Locate every blood parasite and identify its species.
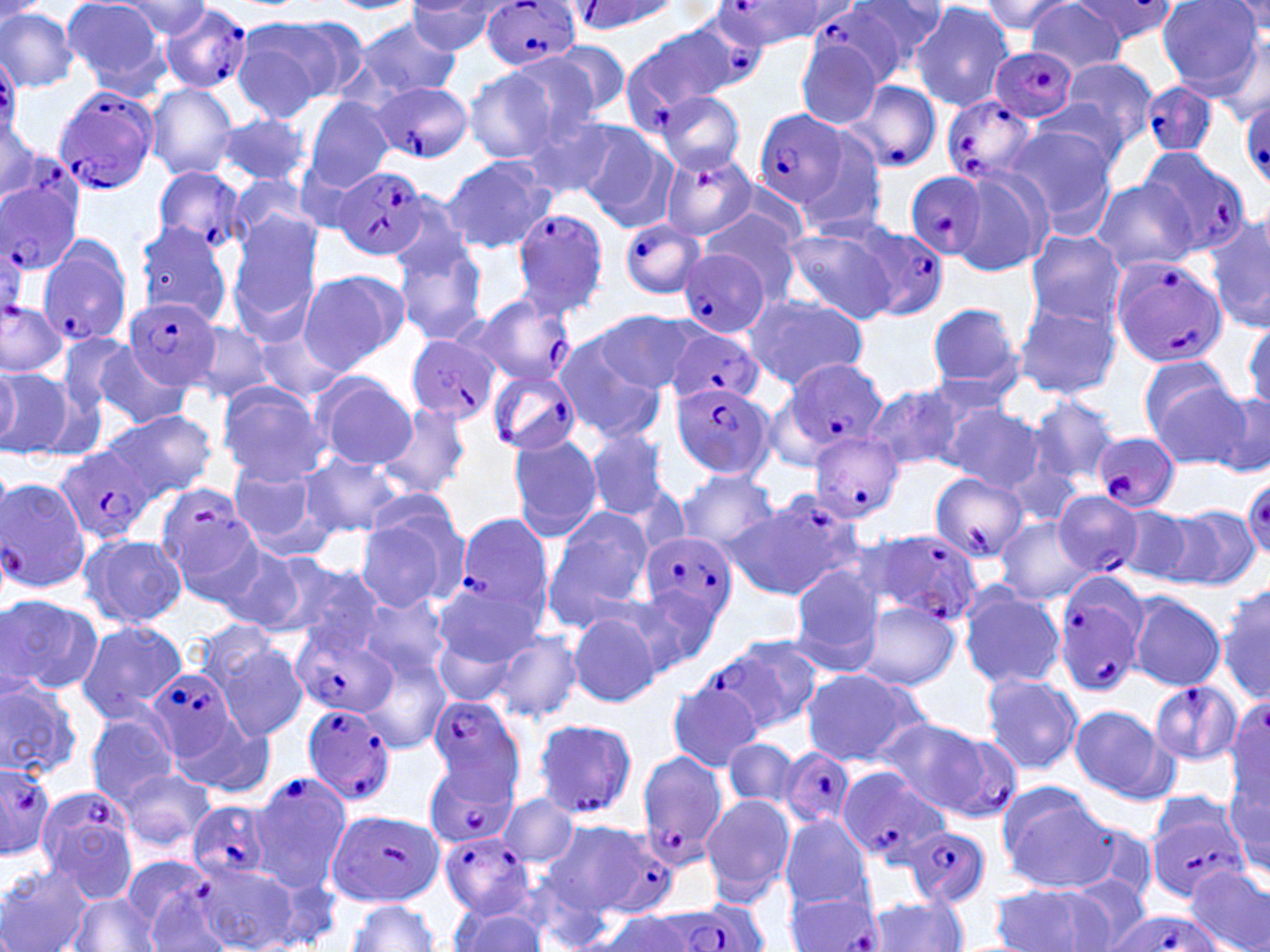

Approximate bounding boxes as (x1, y1, x2, y2) in pixels.
Plasmodium falciparum-infected red blood cells: (719, 0, 830, 50), (571, 1, 680, 33), (484, 2, 581, 72), (157, 5, 253, 94), (811, 6, 909, 87), (679, 10, 769, 93), (621, 27, 737, 124), (988, 47, 1079, 124), (0, 54, 22, 139), (843, 79, 943, 174), (365, 80, 474, 162), (1142, 81, 1216, 156), (51, 86, 160, 196), (942, 94, 1040, 186), (1239, 95, 1270, 187), (754, 110, 848, 208), (1140, 148, 1252, 253), (662, 152, 757, 242), (152, 166, 250, 255), (334, 168, 428, 260), (2, 169, 85, 277), (903, 172, 985, 262), (512, 208, 609, 318), (618, 219, 707, 301), (848, 224, 949, 319), (0, 230, 26, 325), (36, 236, 132, 348), (678, 247, 770, 337), (1110, 257, 1226, 368), (125, 296, 220, 391), (452, 297, 575, 400), (668, 331, 764, 408), (406, 334, 499, 424), (777, 358, 887, 460), (485, 367, 581, 457), (672, 381, 773, 482), (810, 432, 903, 524), (1093, 432, 1180, 513), (57, 446, 153, 548), (930, 471, 1030, 562), (2, 476, 91, 596), (154, 482, 258, 589), (1053, 491, 1144, 577), (453, 512, 552, 626), (639, 530, 738, 634), (855, 530, 984, 627), (1051, 573, 1147, 697), (292, 627, 396, 719), (717, 635, 824, 735), (146, 668, 241, 762), (1149, 680, 1242, 765), (425, 695, 527, 797), (301, 703, 398, 807), (530, 717, 639, 820), (932, 729, 1023, 824), (779, 749, 855, 830), (635, 750, 727, 870), (0, 760, 56, 856), (424, 761, 517, 849), (838, 770, 952, 866), (249, 773, 351, 890), (35, 785, 139, 902), (187, 800, 273, 882), (1146, 808, 1248, 902), (329, 811, 444, 907), (901, 825, 992, 910), (439, 830, 536, 918), (603, 833, 671, 913), (123, 856, 211, 934), (785, 892, 883, 951), (674, 900, 768, 952), (1103, 911, 1224, 952).
No Plasmodium ovale, Plasmodium malariae, Plasmodium vivax, Babesia divergens, or Trypanosoma brucei observed.

slide-level diagnosis = Plasmodium falciparum
magnification = 1000x
preparation = thin blood film
modality = optical microscopy
uninfected red blood cell locations = approximate bounding boxes as (x1, y1, x2, y2) in pixels: (854, 0, 951, 77), (979, 0, 1076, 35), (1157, 0, 1265, 95), (61, 1, 171, 94), (113, 1, 215, 40), (325, 1, 419, 13), (1027, 1, 1129, 76), (1227, 1, 1270, 41), (405, 2, 507, 56), (911, 2, 1015, 110), (0, 7, 80, 91), (352, 16, 463, 100), (231, 18, 351, 117), (543, 41, 631, 120), (795, 41, 883, 128), (502, 52, 609, 145), (1056, 57, 1160, 152), (462, 68, 561, 164), (145, 82, 240, 179), (656, 92, 746, 174), (1031, 94, 1135, 181), (303, 96, 394, 192), (510, 106, 619, 198), (214, 112, 311, 187), (1, 117, 41, 201), (574, 123, 675, 228), (787, 125, 890, 238), (1004, 125, 1117, 230), (441, 155, 556, 255), (952, 167, 1053, 277), (228, 174, 316, 250), (1091, 179, 1198, 273), (700, 209, 799, 298), (227, 213, 323, 335), (1208, 214, 1270, 333), (134, 221, 234, 324), (778, 223, 900, 326), (1024, 228, 1124, 326), (394, 237, 488, 346), (297, 268, 408, 371), (740, 291, 869, 389), (1014, 298, 1121, 400), (926, 302, 1025, 395), (591, 311, 700, 393), (1245, 319, 1270, 412), (185, 320, 279, 404), (250, 324, 351, 404), (55, 331, 139, 418), (551, 334, 666, 442), (88, 342, 194, 429), (1137, 356, 1242, 454), (0, 364, 21, 447), (1, 369, 77, 461), (312, 372, 417, 470), (216, 381, 330, 485), (1158, 382, 1265, 471), (863, 383, 963, 474), (1209, 388, 1270, 476), (1028, 395, 1119, 486), (374, 402, 473, 500), (941, 405, 1047, 493), (104, 408, 218, 500), (585, 429, 670, 520), (506, 433, 604, 542), (301, 453, 404, 537), (1003, 459, 1082, 528), (226, 461, 329, 552), (676, 470, 779, 552), (734, 491, 866, 600), (354, 503, 469, 612), (544, 505, 652, 625), (1113, 505, 1212, 588), (1162, 505, 1260, 587), (995, 519, 1095, 605), (79, 533, 187, 629), (209, 541, 321, 635), (266, 558, 384, 653), (790, 567, 885, 669), (432, 579, 542, 672), (1216, 579, 1270, 706), (958, 585, 1066, 690), (627, 586, 719, 672), (1125, 591, 1226, 691), (0, 592, 102, 697), (358, 594, 450, 686), (856, 601, 960, 691), (566, 606, 667, 706), (74, 620, 188, 722), (433, 626, 520, 707), (201, 628, 309, 742), (492, 630, 581, 724), (359, 648, 451, 754), (799, 668, 927, 766), (980, 672, 1082, 774), (0, 676, 84, 780), (665, 679, 767, 771), (1068, 706, 1177, 807), (85, 710, 180, 807), (173, 712, 279, 799), (873, 718, 999, 815), (722, 737, 801, 808), (116, 766, 216, 855), (1227, 777, 1270, 881), (996, 787, 1116, 890), (499, 792, 578, 868), (699, 794, 795, 902), (778, 816, 873, 908), (541, 819, 643, 919), (191, 861, 297, 951), (0, 864, 95, 952), (1186, 865, 1270, 952), (527, 872, 624, 951), (1068, 874, 1150, 948), (265, 875, 340, 946), (142, 880, 233, 952), (988, 883, 1120, 952), (69, 894, 162, 951), (864, 895, 967, 951), (346, 899, 439, 951), (449, 903, 548, 951), (598, 909, 705, 951)
field of view = single
image size = 1270×952 pixels
stain = May-Grünwald-Giemsa